Outline each uninfected red blood cell.
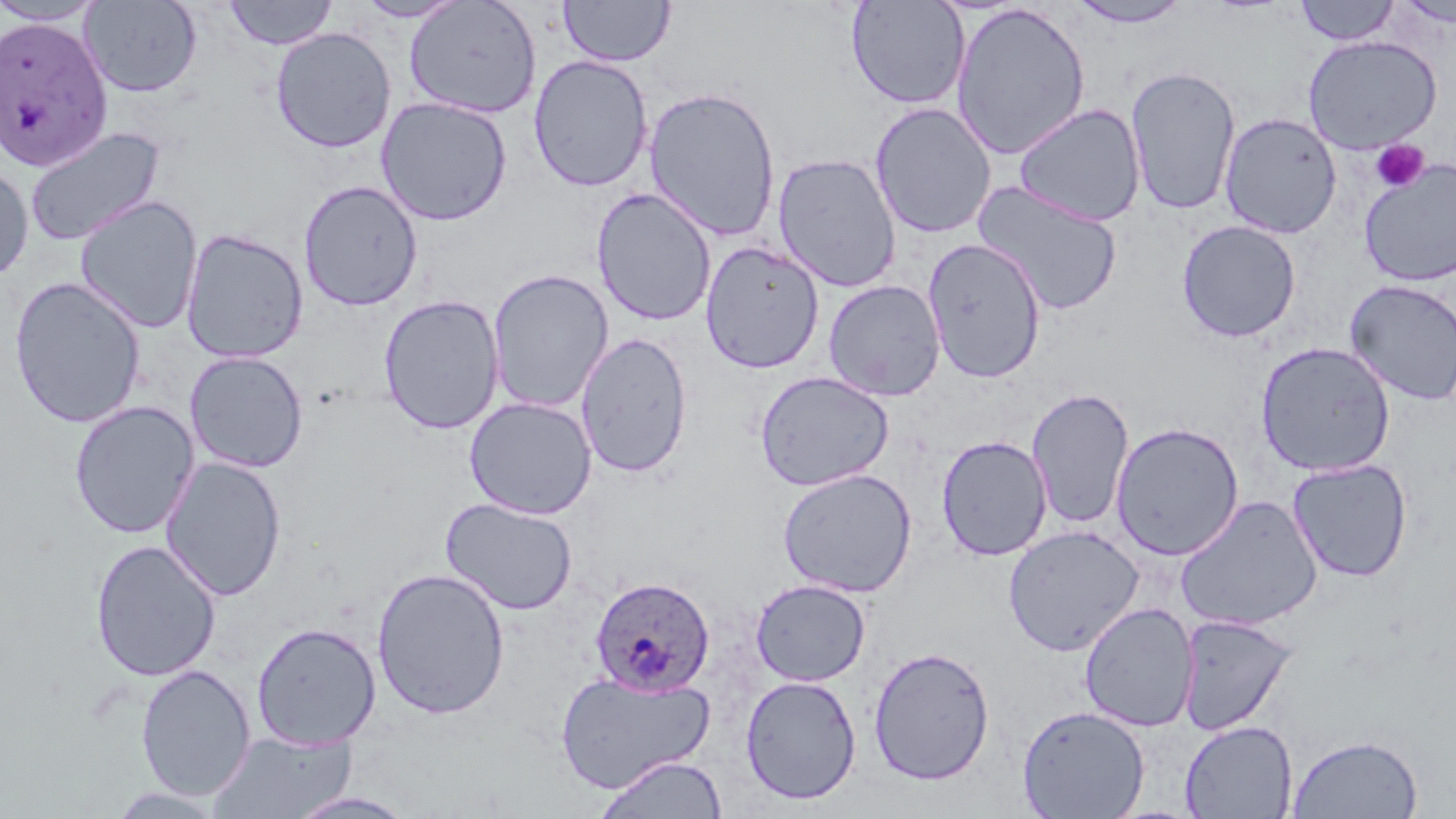
Approximate bounding boxes as (x1, y1, x2, y2) in pixels.
Uninfected red blood cells: (0, 0, 107, 26), (80, 0, 202, 97), (224, 0, 338, 50), (354, 0, 467, 22), (403, 0, 542, 119), (846, 0, 970, 110), (1066, 0, 1194, 28), (1294, 0, 1401, 46), (558, 1, 676, 67), (1396, 1, 1456, 27), (951, 2, 1091, 161), (270, 27, 396, 153), (1303, 35, 1442, 154), (529, 54, 653, 192), (1125, 64, 1242, 216), (643, 86, 781, 242), (376, 96, 512, 226), (869, 102, 997, 239), (1013, 103, 1147, 227), (1219, 112, 1343, 239), (25, 126, 166, 247), (772, 152, 902, 292), (1359, 158, 1456, 287), (0, 163, 34, 282), (971, 179, 1124, 317), (298, 180, 422, 311), (591, 188, 718, 326), (75, 195, 203, 333), (1176, 219, 1301, 343), (180, 228, 309, 363), (922, 238, 1047, 384), (700, 241, 824, 373), (487, 268, 614, 413), (9, 276, 146, 428), (823, 279, 947, 401), (1344, 279, 1456, 405), (378, 294, 504, 435), (575, 332, 693, 477), (1255, 341, 1396, 476), (184, 351, 309, 473), (755, 370, 894, 491), (1026, 386, 1135, 531), (464, 397, 597, 519), (68, 401, 200, 539), (1110, 422, 1244, 560), (936, 435, 1052, 561), (160, 456, 287, 602), (1287, 458, 1413, 582), (778, 467, 918, 597), (1175, 495, 1323, 632), (440, 497, 578, 616), (1003, 525, 1144, 656), (90, 539, 221, 682), (372, 567, 511, 719), (750, 579, 871, 687), (1079, 602, 1199, 731), (1176, 614, 1298, 735), (251, 622, 382, 750), (867, 645, 996, 785), (135, 664, 256, 801), (556, 668, 715, 793), (739, 675, 862, 805), (1017, 704, 1150, 819), (1179, 720, 1298, 819), (208, 729, 357, 818), (1287, 733, 1424, 818), (594, 754, 728, 818), (102, 786, 231, 818), (285, 791, 420, 818).

Plasmodium ovale-infected red blood cell locations: (1, 16, 112, 171), (590, 575, 715, 697). Platelet locations: (1370, 140, 1430, 193). Slide-level diagnosis: Plasmodium ovale. Captured at 1000x magnification. Image is 1456×819 pixels. May-Grünwald-Giemsa-stained preparation. Optical microscopy. Thin blood smear. Single field of view.